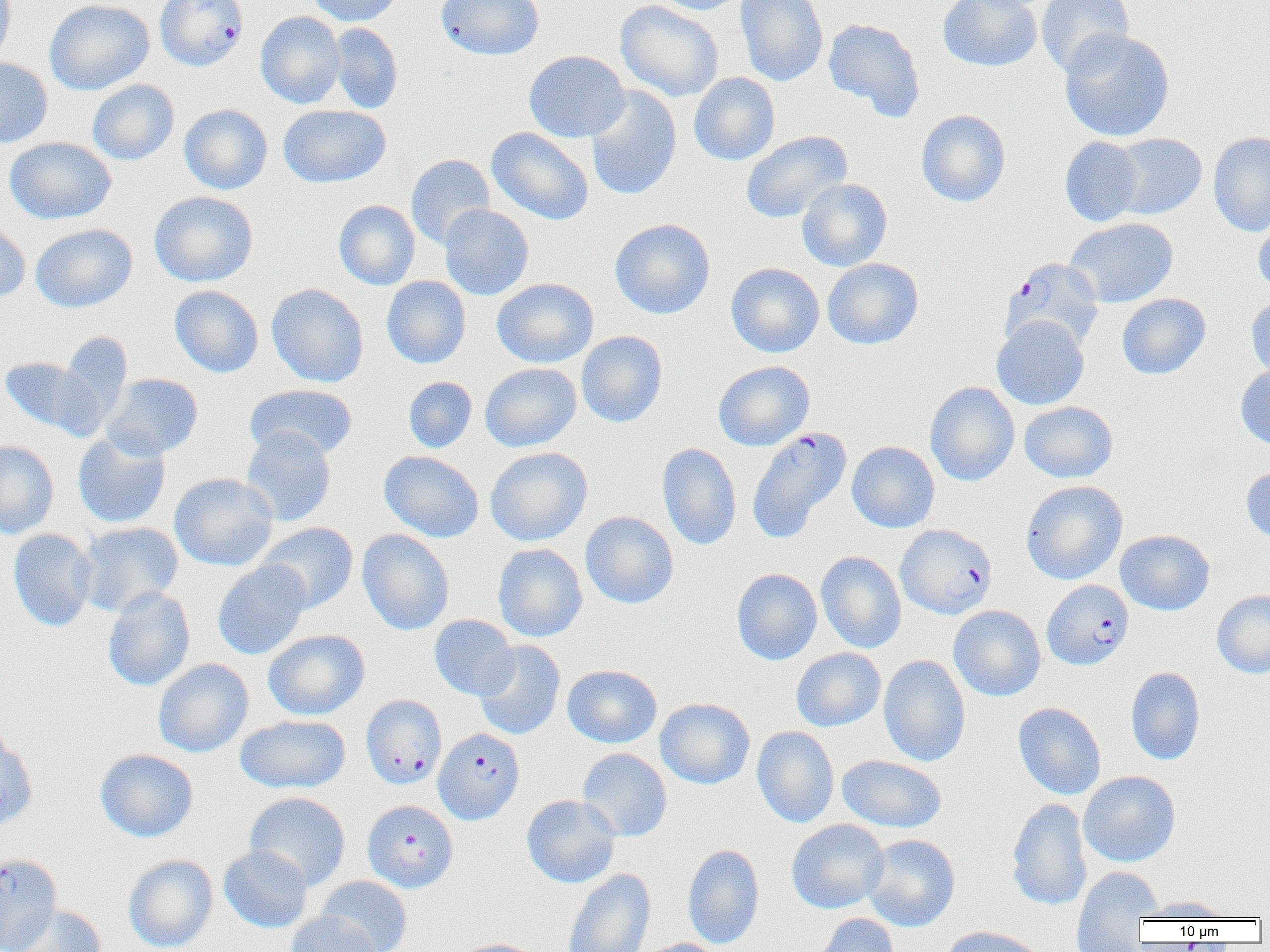
Approximate bounding boxes as (x1,y1)-(x2,y2) corner pairs in pixels. Uninfected red blood cell locations: (0,0)-(16,67), (44,0)-(155,95), (307,0)-(403,26), (436,0)-(544,60), (614,0)-(724,102), (649,0)-(750,15), (735,0)-(828,87), (938,0)-(1042,72), (1036,0)-(1135,77), (256,11)-(345,108), (823,18)-(925,119), (328,23)-(403,113), (1058,29)-(1175,142), (524,50)-(630,142), (0,57)-(53,148), (689,72)-(780,165), (87,80)-(179,165), (585,85)-(682,201), (179,104)-(273,194), (278,104)-(391,188), (916,109)-(1011,207), (486,127)-(594,225), (740,130)-(853,224), (1208,131)-(1270,237), (1109,132)-(1207,220), (1060,136)-(1145,227), (5,137)-(116,224), (406,154)-(495,249), (797,178)-(892,271), (149,191)-(258,287), (333,199)-(420,290), (439,204)-(533,300), (1253,211)-(1270,295), (1065,217)-(1178,308), (610,218)-(715,319), (0,221)-(31,304), (30,224)-(137,312), (822,257)-(923,349), (725,262)-(824,357), (382,276)-(471,368), (491,277)-(599,367), (266,283)-(369,387), (169,285)-(264,377), (1116,293)-(1210,380), (1246,294)-(1270,382), (991,315)-(1089,410), (576,331)-(668,427), (59,332)-(132,432), (0,356)-(105,439), (713,360)-(815,451), (480,362)-(581,452), (1235,365)-(1270,450), (101,373)-(203,459), (404,376)-(477,453), (924,381)-(1019,486), (244,383)-(358,461), (1019,401)-(1118,483), (240,427)-(336,526), (73,430)-(171,528), (0,440)-(59,539), (847,441)-(940,532), (657,443)-(741,550), (485,446)-(592,546), (379,450)-(484,542), (1241,465)-(1270,543), (169,473)-(278,571), (1021,480)-(1127,585), (580,511)-(679,609), (78,521)-(184,615), (256,522)-(359,613), (8,528)-(97,631), (357,529)-(454,635), (1115,530)-(1215,615), (492,543)-(587,642), (816,551)-(906,653), (212,560)-(311,660), (731,568)-(822,665), (103,586)-(195,692), (1211,590)-(1270,678), (948,605)-(1046,701), (429,614)-(519,700), (263,629)-(370,720), (474,640)-(566,740), (791,648)-(886,731), (879,654)-(971,766), (153,658)-(253,757), (562,664)-(662,748), (1126,666)-(1205,765), (655,698)-(755,789), (1013,702)-(1106,800), (235,714)-(351,794), (752,726)-(839,827), (0,732)-(38,830), (577,748)-(672,841), (95,749)-(198,842), (837,754)-(947,833), (1078,770)-(1180,867), (244,792)-(351,891), (521,794)-(621,888), (1006,798)-(1091,911), (786,819)-(889,914), (862,833)-(961,931), (682,844)-(765,949), (218,845)-(312,932), (124,854)-(218,952), (1071,866)-(1162,948), (562,867)-(656,952), (316,876)-(412,952), (1136,896)-(1235,920), (6,904)-(108,952), (285,911)-(381,952), (813,913)-(900,952), (939,925)-(1048,952), (452,938)-(544,952), (634,938)-(728,952). Plasmodium falciparum-infected red blood cell locations: (155,0)-(249,71), (1000,257)-(1104,352), (747,426)-(852,543), (895,524)-(997,619), (1042,579)-(1134,670), (360,694)-(447,789), (434,727)-(524,824), (362,800)-(458,892), (0,853)-(62,952). Slide-level diagnosis: Plasmodium falciparum. Image is 1270×952 pixels. One field of a larger specimen. Optical microscopy. Captured at 1000x magnification. Thin blood film.